Assess for Plasmodium parasites.
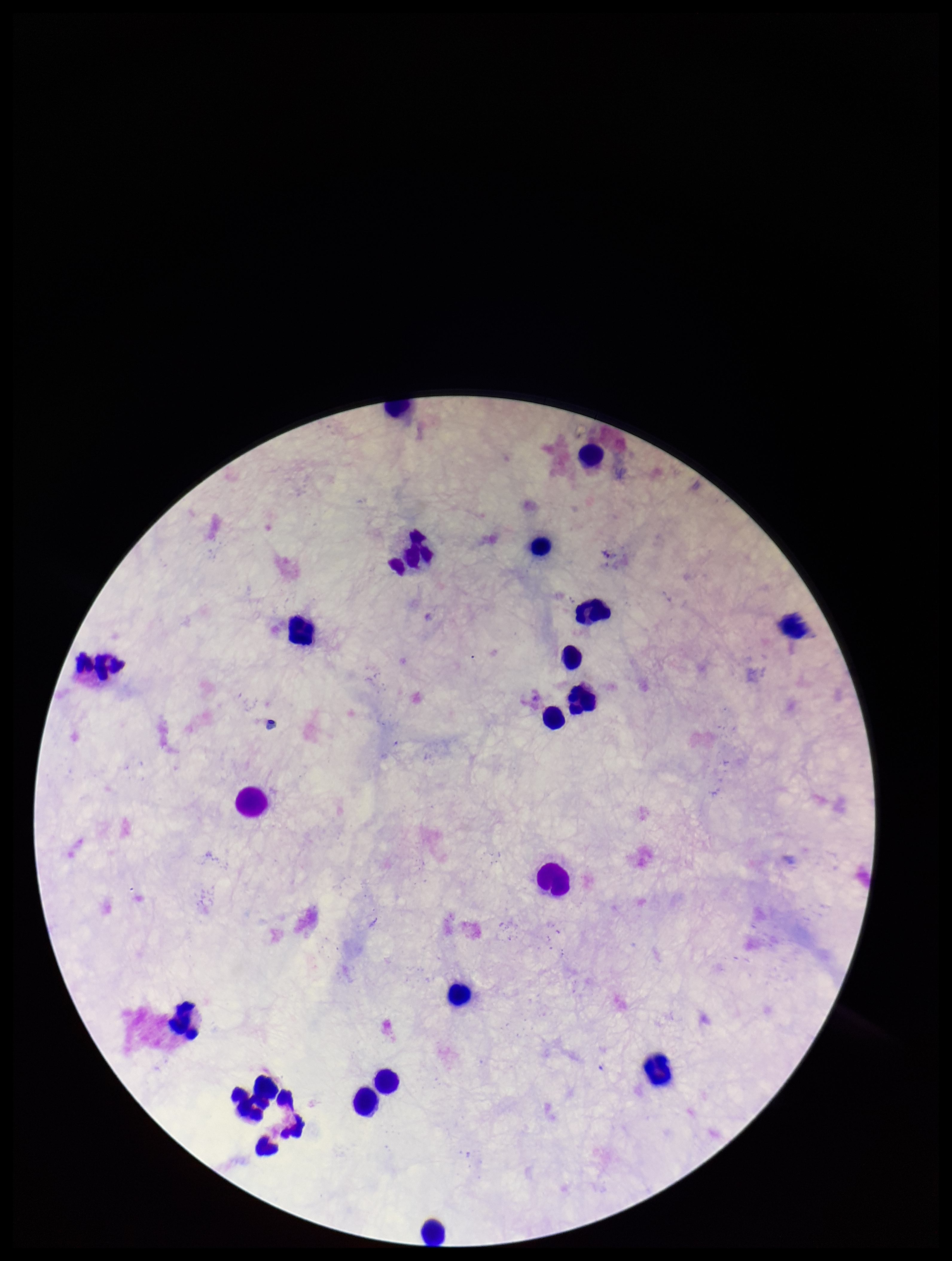
None seen.

leukocyte_count: 21
patient_malaria_status: negative
image_size: 952×1261 pixels
capture: smartphone photograph through the microscope eyepiece
preparation: thick blood smear
field_of_view: one from this slide
stain: Giemsa
parasite_count: 0